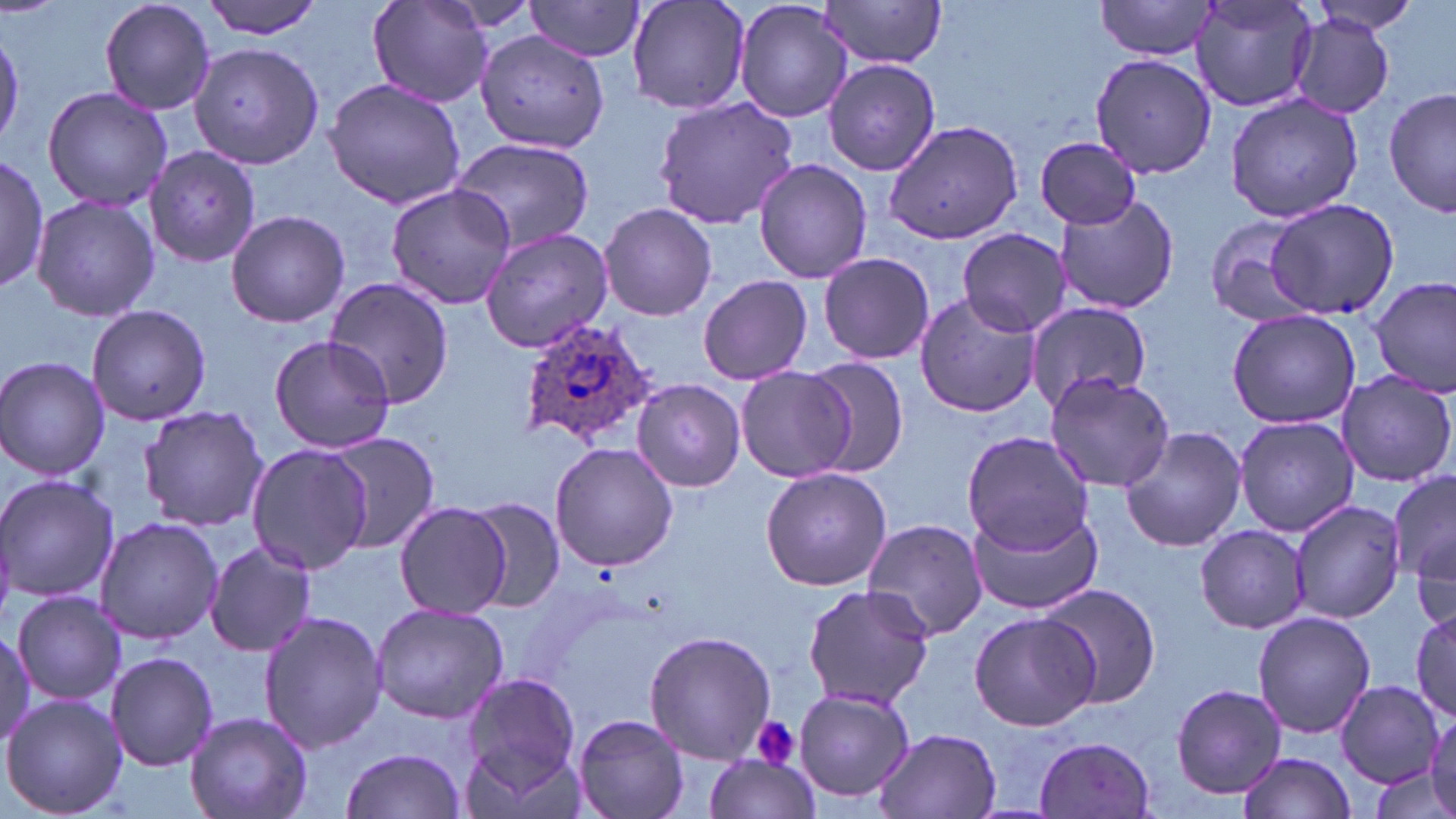
Approximate bounding boxes as (x1, y1, x2, y2) in pixels. Plasmodium ovale-infected red blood cell locations: (517, 319, 659, 452). Uninfected red blood cell locations: (97, 0, 216, 116), (202, 0, 329, 39), (368, 0, 494, 107), (627, 0, 751, 116), (733, 0, 854, 123), (815, 0, 950, 69), (1094, 0, 1221, 60), (1189, 0, 1321, 112), (523, 1, 647, 62), (1305, 1, 1424, 38), (1288, 14, 1396, 120), (0, 24, 26, 153), (474, 29, 609, 153), (189, 41, 327, 170), (1089, 51, 1216, 178), (824, 57, 941, 177), (322, 78, 467, 211), (40, 86, 173, 212), (1385, 88, 1455, 218), (1225, 93, 1362, 223), (653, 97, 801, 228), (883, 117, 1027, 246), (1033, 135, 1143, 230), (447, 138, 595, 252), (145, 144, 266, 265), (0, 157, 47, 295), (753, 159, 874, 283), (385, 184, 519, 309), (30, 194, 159, 321), (1053, 195, 1179, 317), (1266, 198, 1398, 319), (598, 204, 718, 320), (225, 208, 350, 328), (1203, 214, 1321, 326), (478, 226, 617, 352), (957, 228, 1070, 337), (817, 252, 936, 366), (698, 273, 813, 384), (1371, 276, 1455, 392), (323, 278, 454, 408), (914, 293, 1039, 419), (1023, 300, 1152, 413), (84, 304, 213, 425), (1226, 308, 1361, 428), (268, 335, 397, 454), (0, 356, 112, 481), (800, 356, 910, 478), (735, 366, 854, 483), (1045, 372, 1174, 492), (1336, 373, 1454, 488), (630, 378, 747, 492), (137, 405, 268, 533), (1233, 415, 1358, 536), (1121, 425, 1246, 552), (961, 430, 1096, 557), (324, 431, 442, 555), (549, 443, 678, 571), (247, 444, 373, 575), (760, 466, 892, 592), (1387, 466, 1455, 595), (0, 474, 119, 608), (466, 497, 566, 612), (1292, 499, 1406, 623), (393, 501, 513, 618), (967, 503, 1104, 617), (1406, 503, 1454, 633), (94, 517, 224, 645), (863, 518, 988, 642), (1196, 523, 1308, 633), (203, 542, 318, 659), (1036, 581, 1166, 711), (801, 583, 934, 711), (12, 589, 125, 706), (370, 604, 508, 723), (1412, 608, 1456, 721), (258, 610, 388, 754), (967, 610, 1100, 732), (1252, 611, 1376, 737), (643, 631, 778, 763), (105, 651, 219, 771), (457, 669, 583, 793), (125, 677, 267, 804), (1336, 680, 1443, 786), (1171, 682, 1286, 800), (793, 688, 916, 804), (2, 694, 127, 818), (184, 711, 313, 819), (571, 713, 691, 819), (874, 727, 1001, 819), (1034, 735, 1157, 817), (339, 745, 468, 819), (1236, 751, 1356, 819), (700, 752, 821, 819), (1370, 766, 1454, 816). Platelet locations: (750, 717, 802, 770). Slide-level diagnosis: Plasmodium ovale. Light microscopy. Image is 1456×819 pixels. Thin blood smear. Captured at 1000x magnification. Single field of view. May-Grünwald-Giemsa stain.